Give the preparation type.
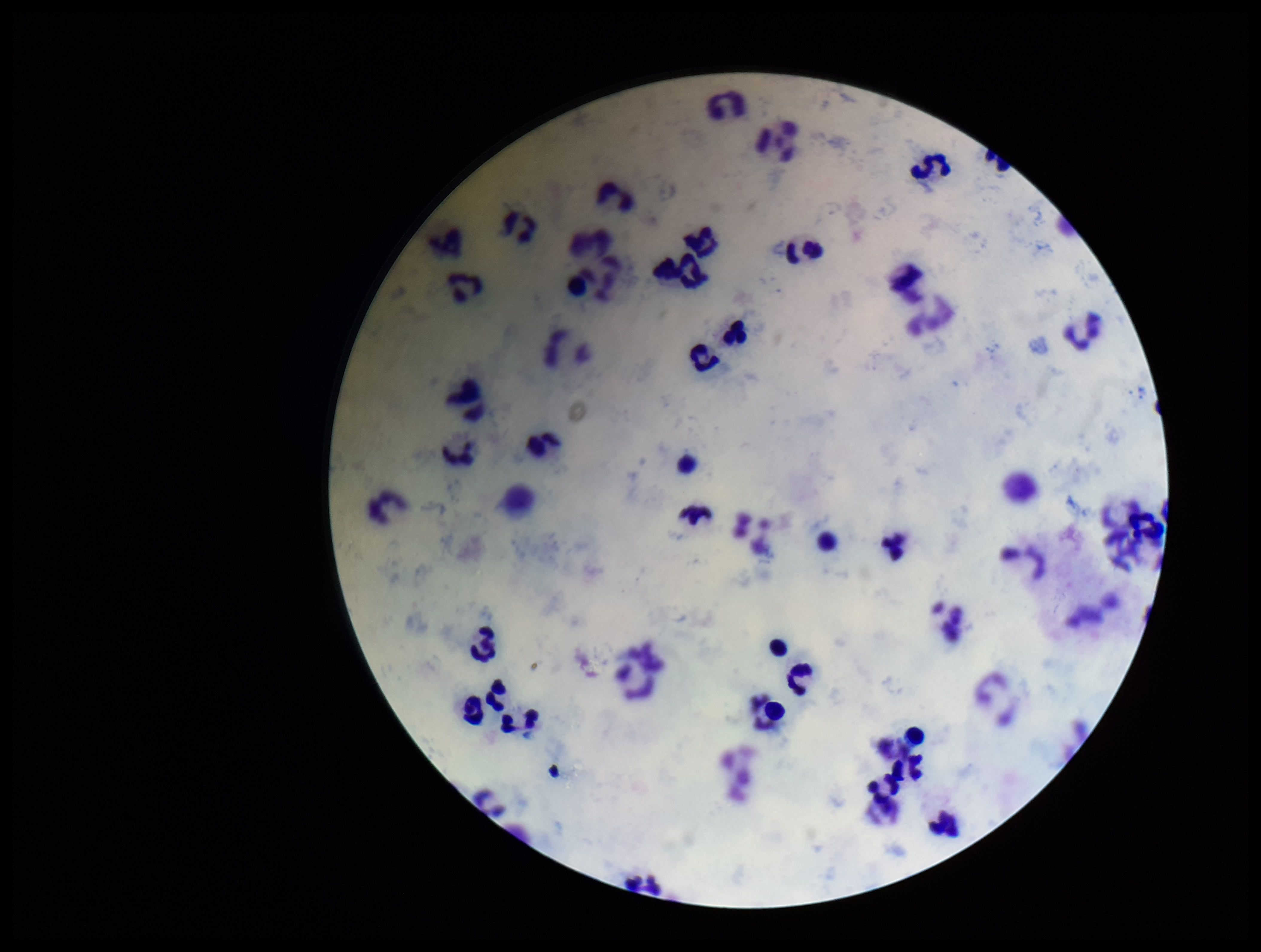

Thick.

Parasite count: 0. Plasmodium parasites: none detected. Smartphone photograph taken through the eyepiece of a microscope. Stained with Giemsa. Patient malaria status: negative. Leukocyte count: 46. Image is 1261×952 pixels. Single field of view.